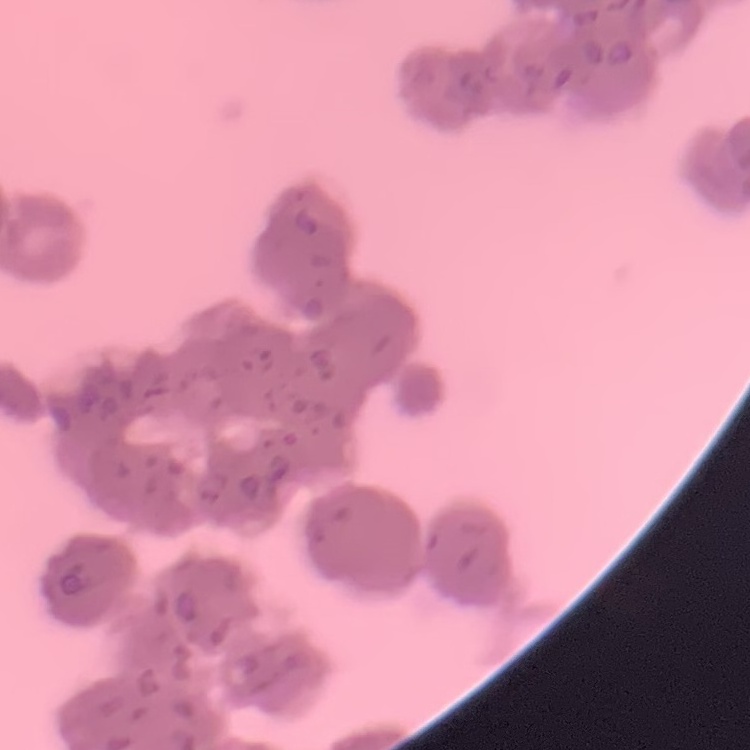

Summary:
  - Red blood cell morphology: rouleaux formation
  - Stain: Field's or Giemsa
  - Preparation: thin blood smear
  - Image type: square crop of a larger photomicrograph